Assess this cell for malaria.
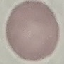
Uninfected.

Giemsa stain. Acquired by smartphone through the microscope eyepiece. Thin blood smear. Cell patch, automatically extracted from a larger field of view and resized to 64 × 64 pixels.